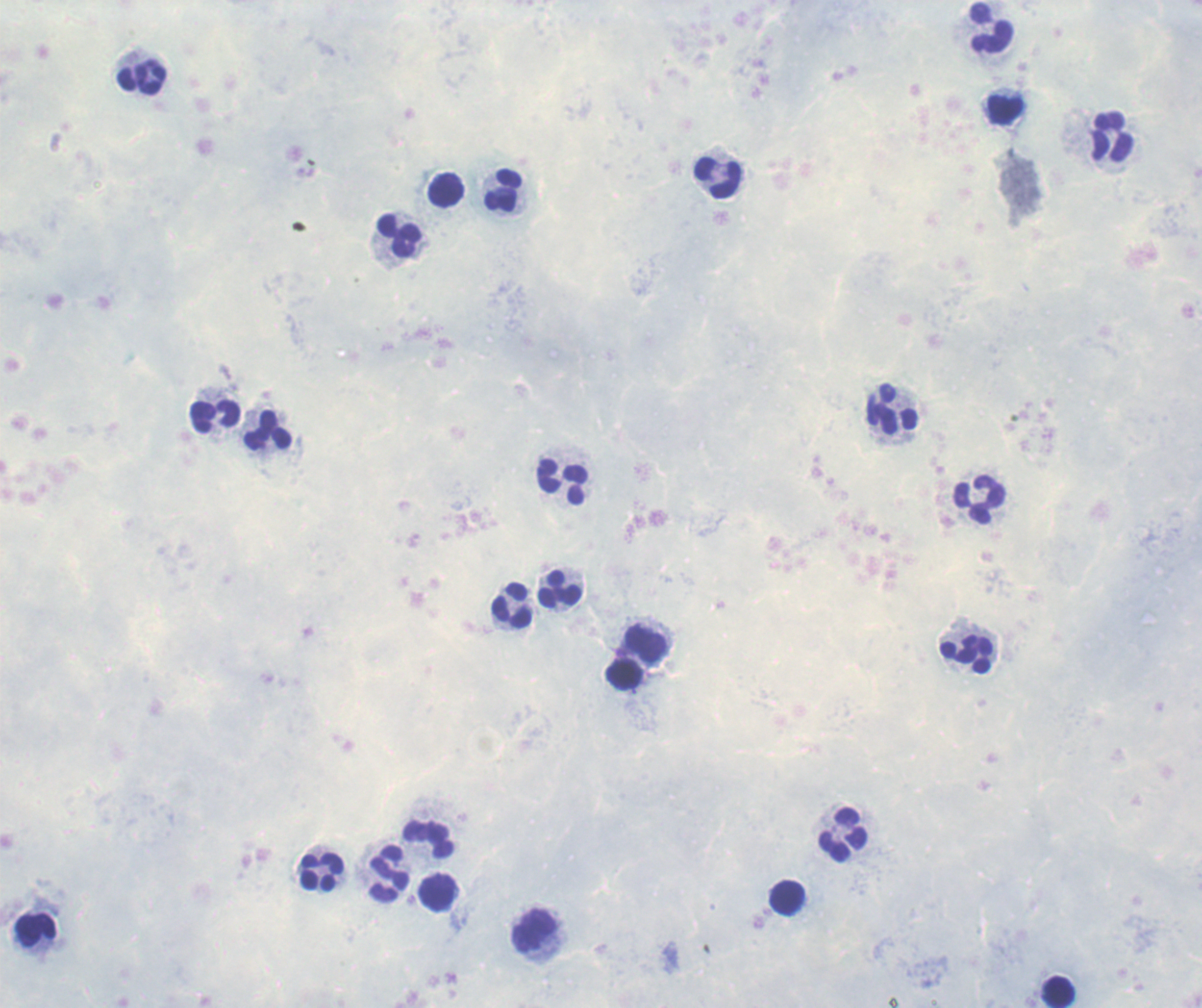

leukocyte_locations: 'approximate centers as {x, y} in pixels: {991, 29}, {142, 76}, {1005, 108}, {1111, 136}, {718, 177}, {446, 189}, {504, 190}, {398, 236}, {893, 410}, {213, 415}, {269, 431}, {562, 481}, {979, 499}, {560, 589}, {514, 605}, {649, 643}, {967, 654}, {626, 675}, {843, 835}, {430, 839}, {321, 873}, {390, 875}, {438, 892}, {788, 897}, {36, 930}, {536, 932}, {1057, 992}'
result: no malaria parasites detected
preparation: thick blood smear
image_size: 1202×1008 pixels
context: previously used in an actual diagnosis
background_quality: poor
magnification: 100x
field_of_view: one from this slide
stain: Romanowsky